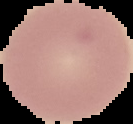
Summary:
  - Malaria status: uninfected
  - Image type: segmented cell region with the area outside set to black
  - Image size: 133×124 pixels
  - Preparation: thin blood smear